Assess the morphology of the red blood cells.
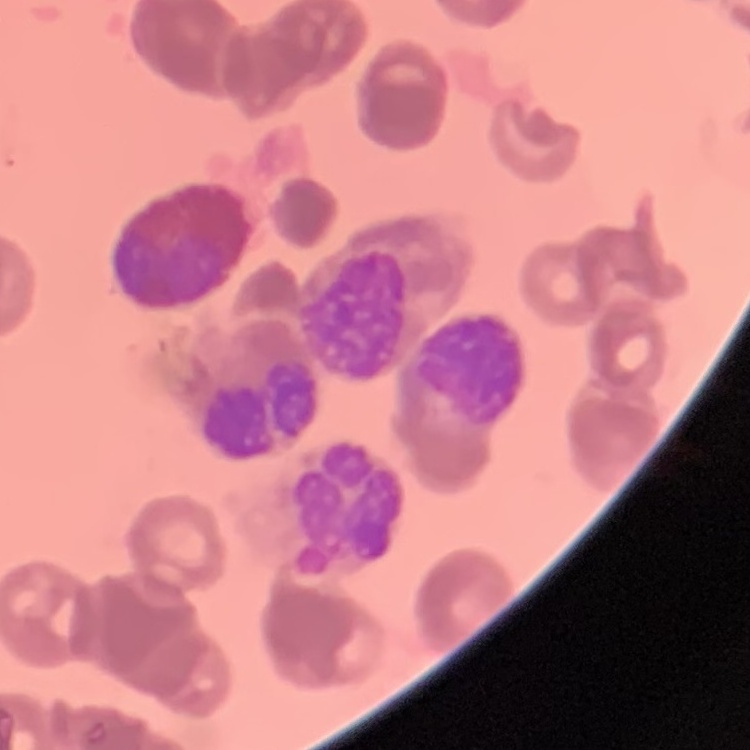
They show rouleaux formation.

preparation = thin peripheral smear
stain = Field's or Giemsa
image type = one tile cut from a larger photomicrograph